Name the blood parasite species.
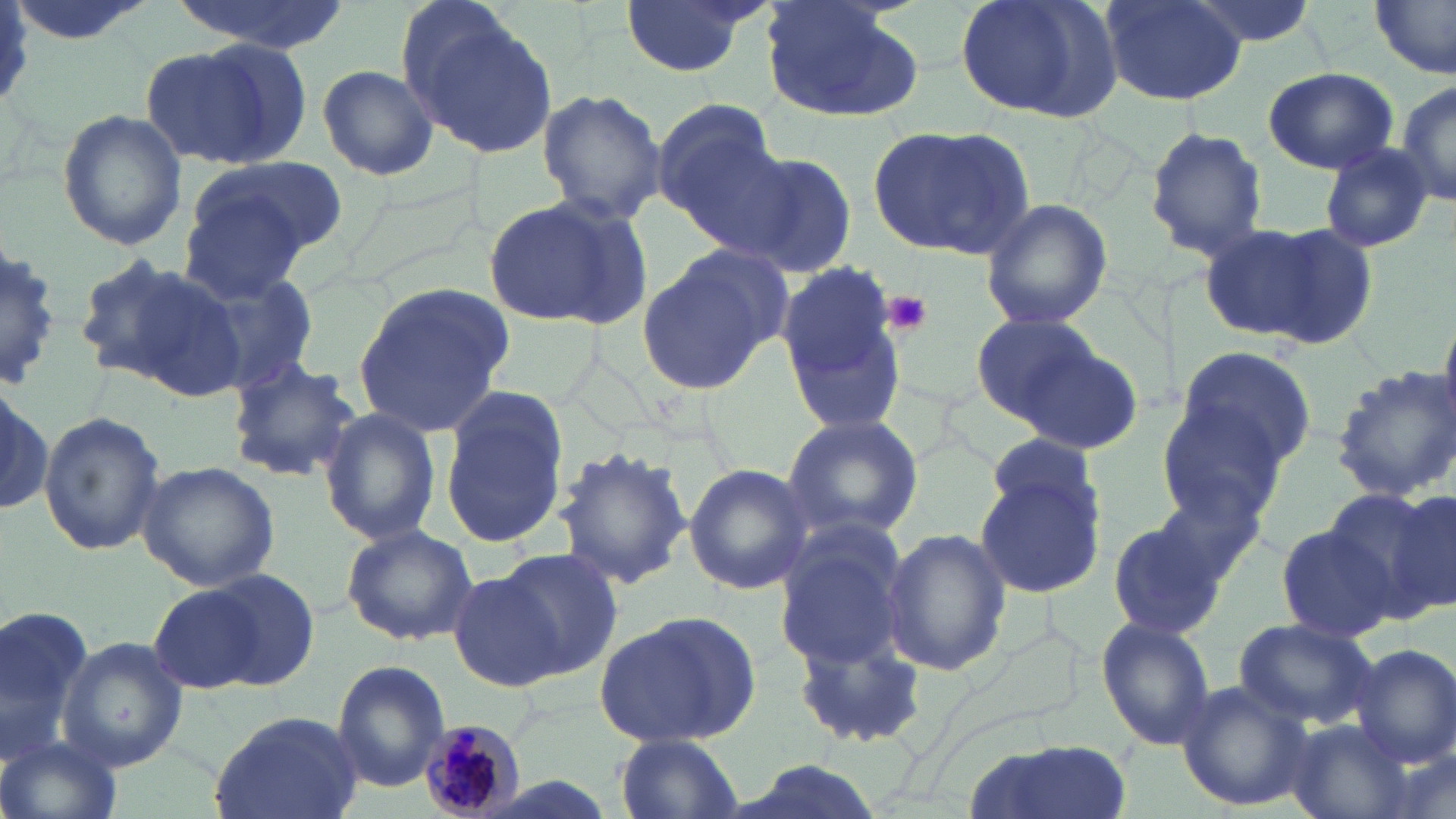
Plasmodium malariae.

stain = May-Grünwald-Giemsa
platelet locations = approximate bounding boxes as [x1, y1, x2, y2] in pixels: [884, 289, 932, 335]
magnification = 1000x
field of view = one of a larger specimen
image size = 1456×819 pixels
modality = optical microscopy
Plasmodium malariae-infected red blood cell locations = approximate bounding boxes as [x1, y1, x2, y2] in pixels: [418, 718, 527, 817]
uninfected red blood cell locations = approximate bounding boxes as [x1, y1, x2, y2] in pixels: [4, 0, 156, 49], [169, 0, 347, 56], [615, 0, 769, 80], [955, 0, 1126, 123], [1102, 0, 1245, 105], [1178, 0, 1324, 47], [760, 2, 922, 123], [1372, 2, 1456, 77], [405, 13, 557, 159], [145, 39, 306, 169], [315, 61, 441, 182], [1263, 67, 1398, 174], [1393, 78, 1456, 210], [536, 88, 667, 223], [652, 99, 786, 238], [56, 109, 188, 252], [868, 121, 1035, 259], [1146, 126, 1270, 259], [1316, 142, 1436, 255], [729, 150, 859, 277], [194, 157, 345, 263], [180, 191, 314, 303], [483, 194, 649, 329], [980, 197, 1113, 331], [1210, 222, 1371, 348], [635, 245, 786, 396], [0, 247, 64, 389], [76, 255, 242, 394], [182, 262, 322, 393], [775, 264, 908, 431], [351, 281, 519, 438], [970, 312, 1106, 426], [1011, 341, 1146, 455], [1167, 343, 1317, 484], [224, 356, 363, 482], [1329, 367, 1456, 506], [0, 374, 49, 524], [439, 387, 568, 549], [1160, 401, 1294, 530], [317, 408, 442, 546], [39, 410, 167, 556], [781, 414, 922, 540], [988, 433, 1100, 526], [554, 443, 692, 589], [137, 460, 282, 592], [1157, 460, 1280, 580], [684, 464, 813, 597], [974, 468, 1104, 600], [1339, 485, 1454, 616], [769, 515, 913, 671], [1104, 516, 1228, 640], [1274, 521, 1398, 642], [340, 524, 479, 646], [880, 526, 1011, 678], [495, 548, 623, 678], [152, 570, 311, 693], [448, 571, 563, 691], [1, 604, 97, 767], [594, 612, 761, 750], [1095, 616, 1216, 750], [1232, 616, 1376, 730], [787, 618, 933, 755], [58, 638, 186, 771], [1350, 643, 1456, 768], [331, 660, 449, 794], [1173, 678, 1315, 813], [208, 711, 365, 819], [1281, 720, 1412, 819], [615, 733, 744, 818], [1, 734, 124, 819], [962, 738, 1134, 819], [724, 758, 892, 819]
preparation = thin blood film